State the blood parasite species.
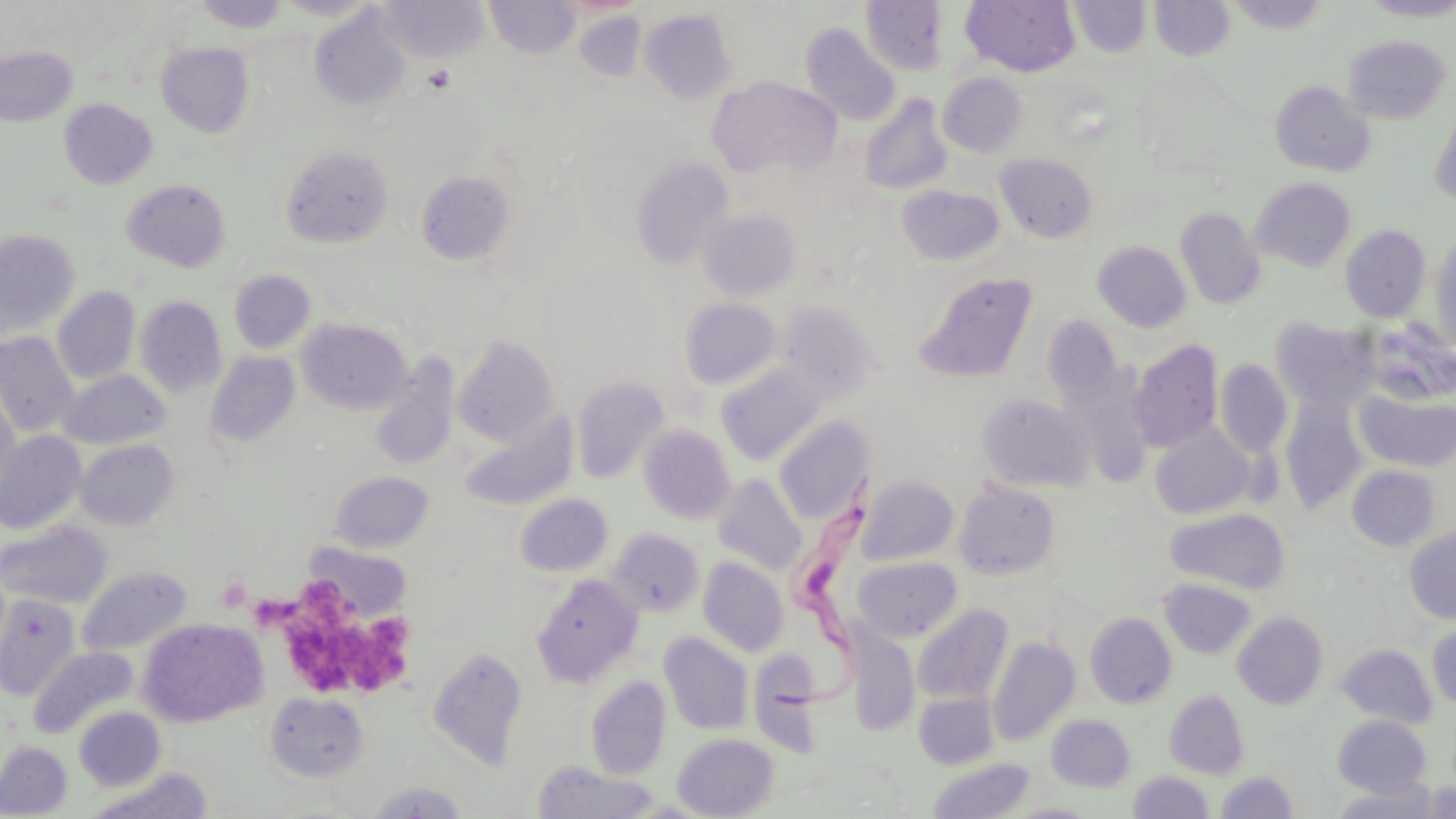

Trypanosoma brucei.

stain = May-Grünwald-Giemsa
platelet locations = approximate bounding boxes as (x1,y1)-(x2,y2) corner pairs in pixels: (425,64)-(456,92), (299,574)-(357,636), (216,578)-(251,612), (342,621)-(418,698), (292,631)-(370,691)
field of view = one of a larger specimen
image size = 1456×819 pixels
modality = light microscopy
Trypanosoma brucei locations = approximate bounding boxes as (x1,y1)-(x2,y2) corner pairs in pixels: (770,479)-(892,715)
uninfected red blood cell locations = approximate bounding boxes as (x1,y1)-(x2,y2) corner pairs in pixels: (274,0)-(381,20), (380,0)-(489,61), (486,0)-(580,59), (861,0)-(948,75), (1068,0)-(1152,58), (1150,0)-(1235,60), (1226,0)-(1332,34), (1360,0)-(1456,21), (193,1)-(291,33), (961,1)-(1080,76), (310,8)-(411,111), (640,9)-(737,104), (574,10)-(646,82), (801,23)-(901,126), (1342,35)-(1452,124), (157,42)-(255,137), (0,46)-(77,126), (1133,64)-(1249,177), (938,73)-(1027,157), (707,75)-(842,180), (1270,80)-(1375,177), (859,93)-(952,195), (59,98)-(157,189), (1429,106)-(1456,208), (281,145)-(394,249), (995,153)-(1097,243), (630,157)-(733,270), (415,170)-(514,265), (1251,177)-(1356,271), (121,178)-(231,272), (897,185)-(1004,266), (1175,208)-(1267,310), (699,209)-(801,302), (695,212)-(791,393), (1340,225)-(1431,323), (0,230)-(80,337), (1429,232)-(1456,353), (1093,241)-(1191,332), (229,270)-(315,353), (914,271)-(1037,383), (53,286)-(141,384), (135,295)-(226,398), (679,298)-(781,390), (777,301)-(881,404), (1043,316)-(1124,409), (1271,317)-(1378,412), (298,318)-(413,415), (1361,320)-(1456,406), (0,331)-(79,437), (452,335)-(559,446), (1129,340)-(1222,453), (205,350)-(301,450), (370,359)-(459,471), (1216,359)-(1292,458), (717,363)-(826,466), (58,370)-(170,449), (572,375)-(669,484), (0,384)-(21,500), (1355,390)-(1456,471), (977,394)-(1093,493), (1280,395)-(1368,513), (460,411)-(579,512), (775,417)-(873,525), (639,426)-(736,524), (1150,426)-(1257,520), (0,430)-(87,534), (75,439)-(179,530), (1348,465)-(1440,551), (328,471)-(435,553), (712,474)-(808,576), (857,476)-(959,566), (954,481)-(1061,581), (515,494)-(613,577), (1165,507)-(1291,595), (0,520)-(112,609), (1404,525)-(1456,624), (607,528)-(704,617), (854,556)-(962,642), (699,557)-(789,656), (77,565)-(192,657), (532,574)-(643,688), (1158,578)-(1257,660), (0,594)-(81,701), (913,604)-(1013,705), (1233,611)-(1328,710), (1085,613)-(1177,708), (138,618)-(267,727), (1427,621)-(1456,710), (847,626)-(919,736), (659,632)-(754,735), (988,635)-(1080,746), (1336,644)-(1438,727), (29,646)-(137,738), (428,646)-(528,770), (749,649)-(822,757), (586,676)-(671,781), (1164,689)-(1250,778), (266,692)-(369,781), (914,692)-(998,769), (74,706)-(166,791), (1047,714)-(1136,792), (1333,715)-(1432,797), (673,733)-(779,818), (0,741)-(72,817), (928,758)-(1036,818), (532,762)-(661,818), (88,769)-(213,819), (1128,771)-(1215,818), (1217,771)-(1298,818), (365,781)-(471,818), (1421,781)-(1456,818), (1331,782)-(1442,818), (1008,802)-(1099,818)
preparation = thin blood film
magnification = 1000x